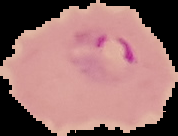

{
  "malaria_status": "parasitized",
  "image_size": "178×136 pixels",
  "preparation": "thin blood smear",
  "image_type": "segmented cell region on a black background"
}